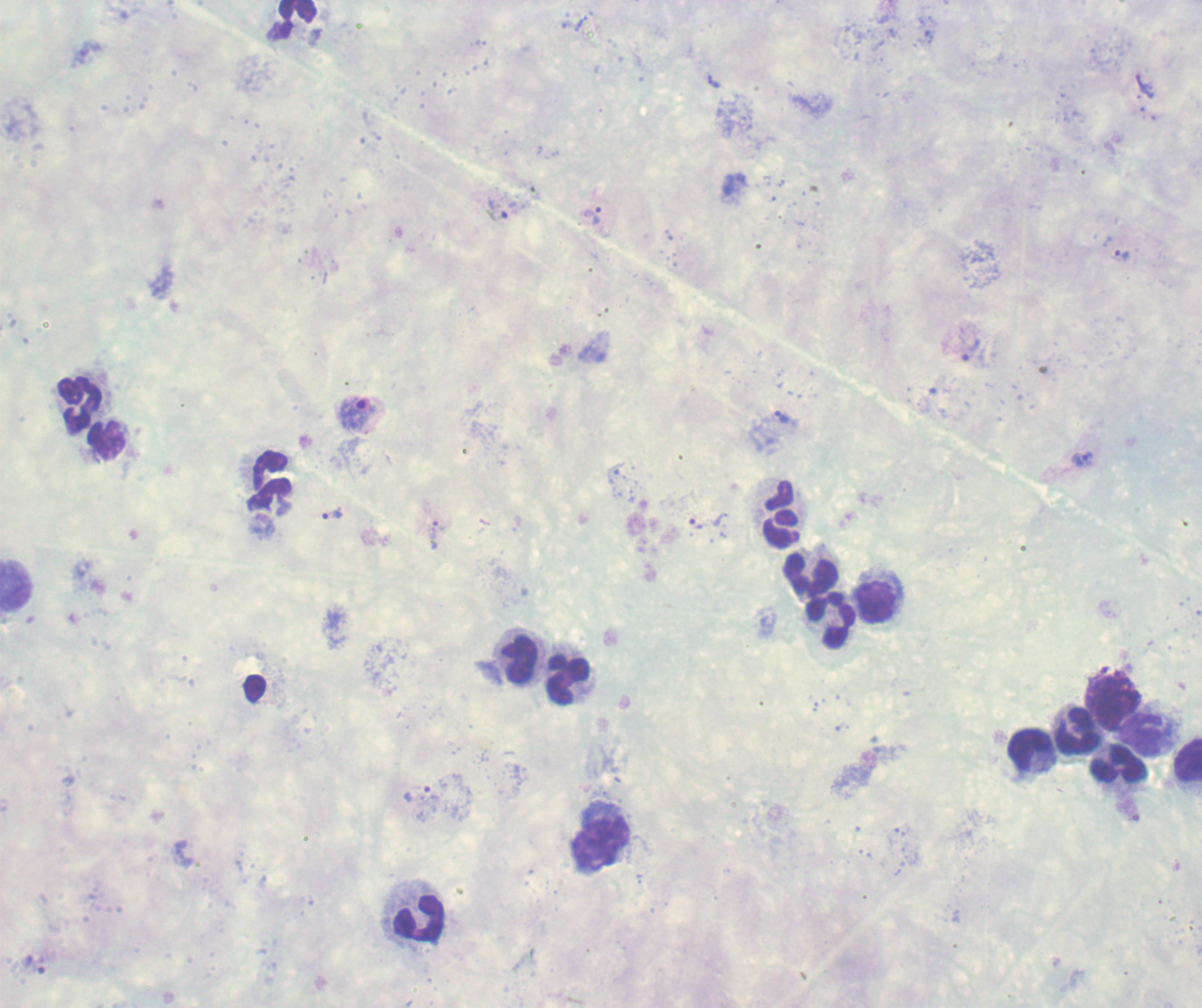
{
  "context": "previously used in an actual diagnosis",
  "image_size": "1202×1008 pixels",
  "trophozoite_locations": "approximate centers as {x, y} in pixels: {714, 82}, {593, 215}, {1122, 255}, {971, 351}, {355, 413}, {782, 418}, {1082, 459}, {333, 513}, {416, 794}",
  "preparation": "thick blood film",
  "result": "malaria parasites detected",
  "stain": "Romanowsky",
  "magnification": "100x",
  "background_quality": "poor",
  "leukocyte_locations": "approximate centers as {x, y} in pixels: {298, 14}, {75, 402}, {107, 439}, {269, 480}, {780, 513}, {809, 574}, {17, 585}, {877, 600}, {831, 622}, {518, 658}, {565, 679}, {254, 689}, {1114, 699}, {1075, 730}, {1143, 734}, {1032, 754}, {1188, 760}, {1115, 767}, {599, 840}, {416, 922}",
  "field_of_view": "one from this slide"
}